Assess this cell for malaria.
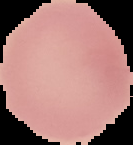

It is uninfected.

preparation = thin blood smear
image type = cell region segmented out of the field of view; surrounding area masked to black
image size = 133×145 pixels